Classify this cell by malaria status.
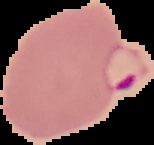

Parasitized.

{
  "preparation": "thin blood film",
  "image_type": "segmented cell region on a black background",
  "image_size": "154×145 pixels"
}